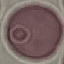
result = no malaria parasites detected
image type = automatically extracted cell patch, resized to 64 × 64 pixels
stain = Giemsa
capture = smartphone through the microscope eyepiece
preparation = thin blood film